Report the malaria status of this cell.
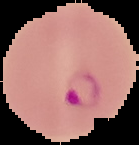
Parasitized.

Summary:
  - Image type: segmented cell region on a black background
  - Preparation: thin blood smear
  - Image size: 139×145 pixels